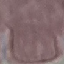
Result: no malaria parasites seen. Thin smear of blood. Acquired by smartphone through the microscope eyepiece. Giemsa-stained preparation. Automatically extracted cell patch, resized to 64 × 64 pixels.